Mark where cells are.
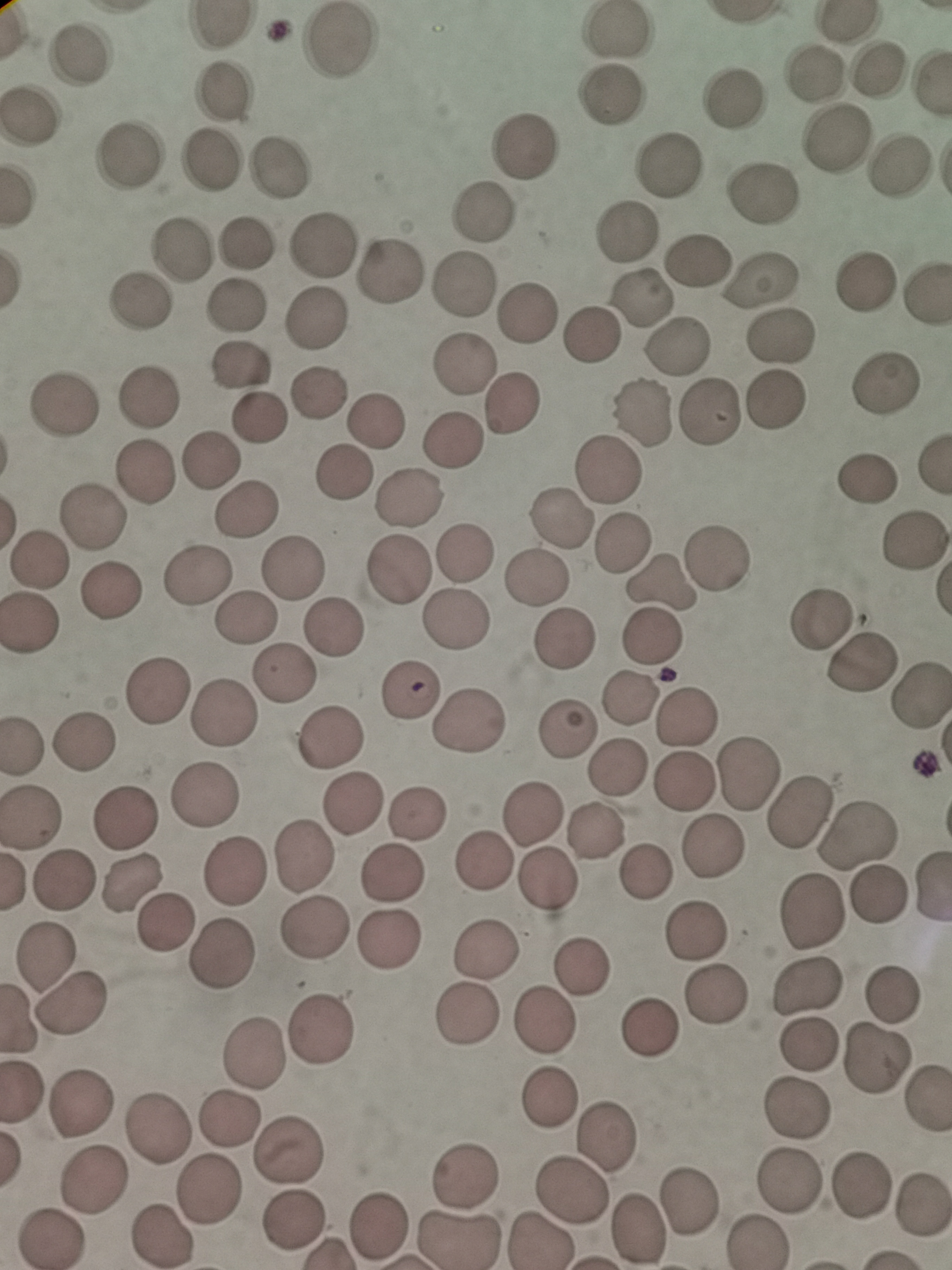
Approximate centers as (x, y) in pixels.
Cells: (614, 31), (337, 43), (79, 55), (879, 70), (815, 74), (225, 90), (610, 95), (738, 98), (28, 117), (837, 138), (529, 147), (134, 155), (213, 165), (671, 165), (277, 166), (898, 168), (761, 197), (485, 211), (626, 234), (245, 242), (322, 244), (180, 248), (697, 261), (393, 270), (763, 277), (466, 281), (866, 286), (927, 296), (639, 297), (141, 299), (235, 306), (529, 310), (314, 315), (593, 336), (776, 336), (674, 345), (463, 366), (240, 367), (884, 385), (320, 389), (148, 395), (774, 400), (64, 403), (513, 408), (706, 410), (640, 413), (258, 417), (376, 422), (454, 442), (212, 462), (146, 471), (609, 471), (342, 476), (867, 478), (409, 500), (248, 510), (559, 517), (94, 518), (910, 540), (623, 544), (467, 551), (40, 557), (718, 558), (291, 566), (400, 569), (198, 575), (537, 578), (661, 580), (111, 591), (244, 617), (455, 622), (823, 622), (32, 624), (335, 625), (654, 635), (565, 636), (858, 665), (283, 675), (155, 689), (410, 690), (629, 696), (922, 697), (684, 714), (221, 715), (465, 724), (568, 731), (336, 737), (86, 738), (618, 769), (747, 771), (686, 782), (207, 797), (353, 806), (793, 812), (534, 813), (417, 814), (32, 817), (123, 817), (597, 830), (859, 833), (717, 848), (302, 858), (487, 866), (234, 870), (392, 870), (647, 870), (64, 877), (550, 881), (129, 882), (878, 896), (810, 912), (167, 922), (315, 929), (698, 930), (387, 937), (44, 950), (484, 951), (222, 954), (579, 962), (807, 988), (717, 996), (894, 999), (72, 1006), (467, 1016), (544, 1019), (650, 1023), (320, 1025), (807, 1043), (254, 1049), (878, 1061), (551, 1099), (798, 1106), (84, 1107), (228, 1118), (162, 1128), (604, 1132), (290, 1151), (468, 1178), (97, 1180), (789, 1180), (863, 1183), (567, 1187), (209, 1190), (689, 1200), (921, 1206), (294, 1222), (377, 1224), (640, 1230), (162, 1236), (48, 1238), (460, 1240).

capture = smartphone camera at the microscope eyepiece
field of view = single
stain = Giemsa
preparation = thin blood film
image size = 952×1270 pixels